Identify the parasite.
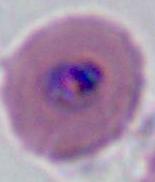

Plasmodium.

Captured at either 400x or 1000x magnification. Micrograph.